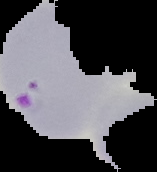

image type = segmented cell region on a black background
preparation = thin blood film
malaria status = parasitized
image size = 157×172 pixels